Comment on the morphology of the erythrocytes.
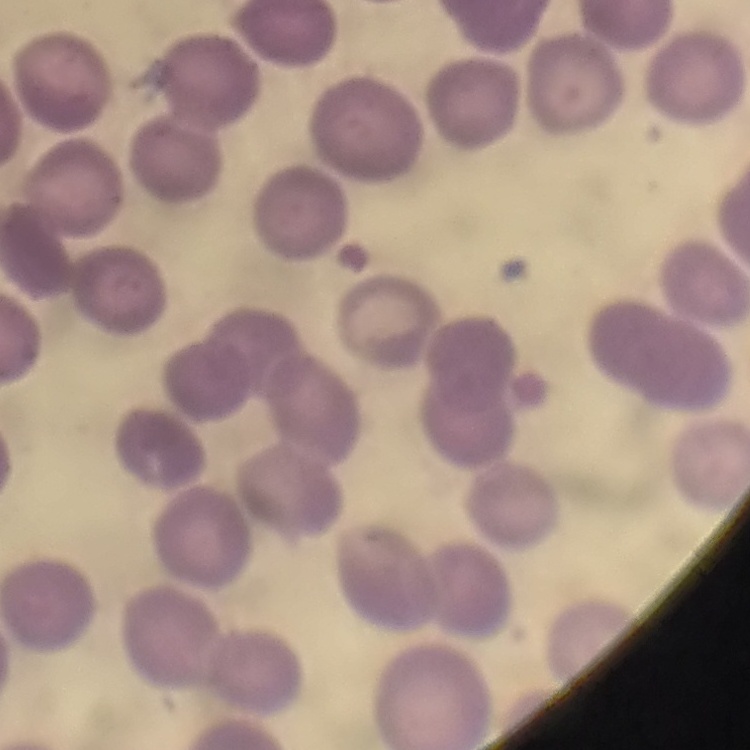

No rouleaux formation.

Thin blood smear. One tile cut from a larger photomicrograph. Stained with either Field's or Giemsa.